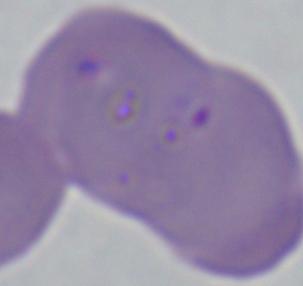

Captured at 1000x magnification. A Babesia parasite is seen. Photomicrograph.